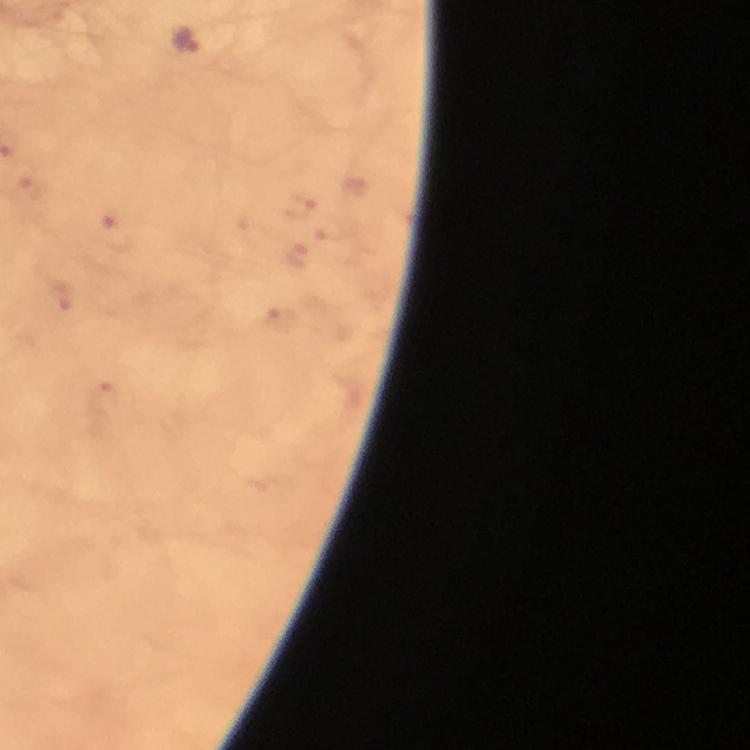

Approximate centers as [x, y] in pixels. Malaria parasite locations: [186, 40], [32, 187], [300, 204], [114, 233], [295, 254], [62, 296], [284, 322], [104, 401]. Image is 750×750 pixels. Immersion oil applied. Photographed with a smartphone mounted on the microscope. From a malaria diagnostic workup. At 100x magnification. Thick smear. Giemsa-stained preparation. A crop from one field of view.